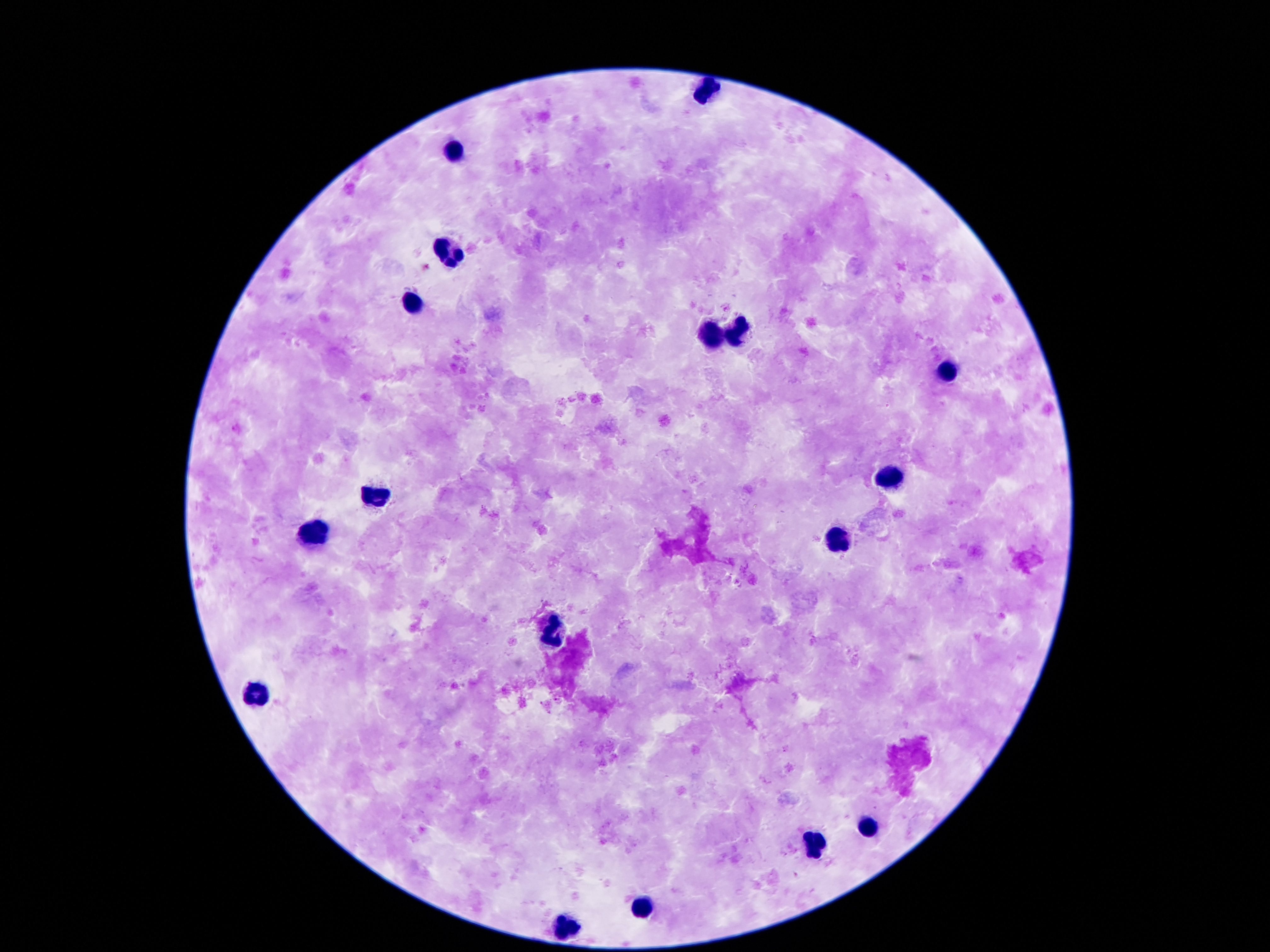
{
  "leukocyte_locations": "approximate centers as {x, y} in pixels: {707, 91}, {455, 151}, {449, 251}, {412, 303}, {737, 331}, {712, 334}, {946, 370}, {890, 478}, {376, 496}, {314, 534}, {836, 538}, {552, 634}, {258, 694}, {869, 830}, {818, 844}, {646, 906}, {569, 924}",
  "stain": "Giemsa",
  "preparation": "thick blood smear",
  "magnification": "100x",
  "image_size": "1270×952 pixels",
  "patient_malaria_status": "not infected",
  "capture": "smartphone camera through the microscope eyepiece",
  "field_of_view": "single"
}